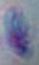
Summary:
  - Magnification: 1000x
  - Identification: Toxoplasma gondii
  - Modality: photomicrograph